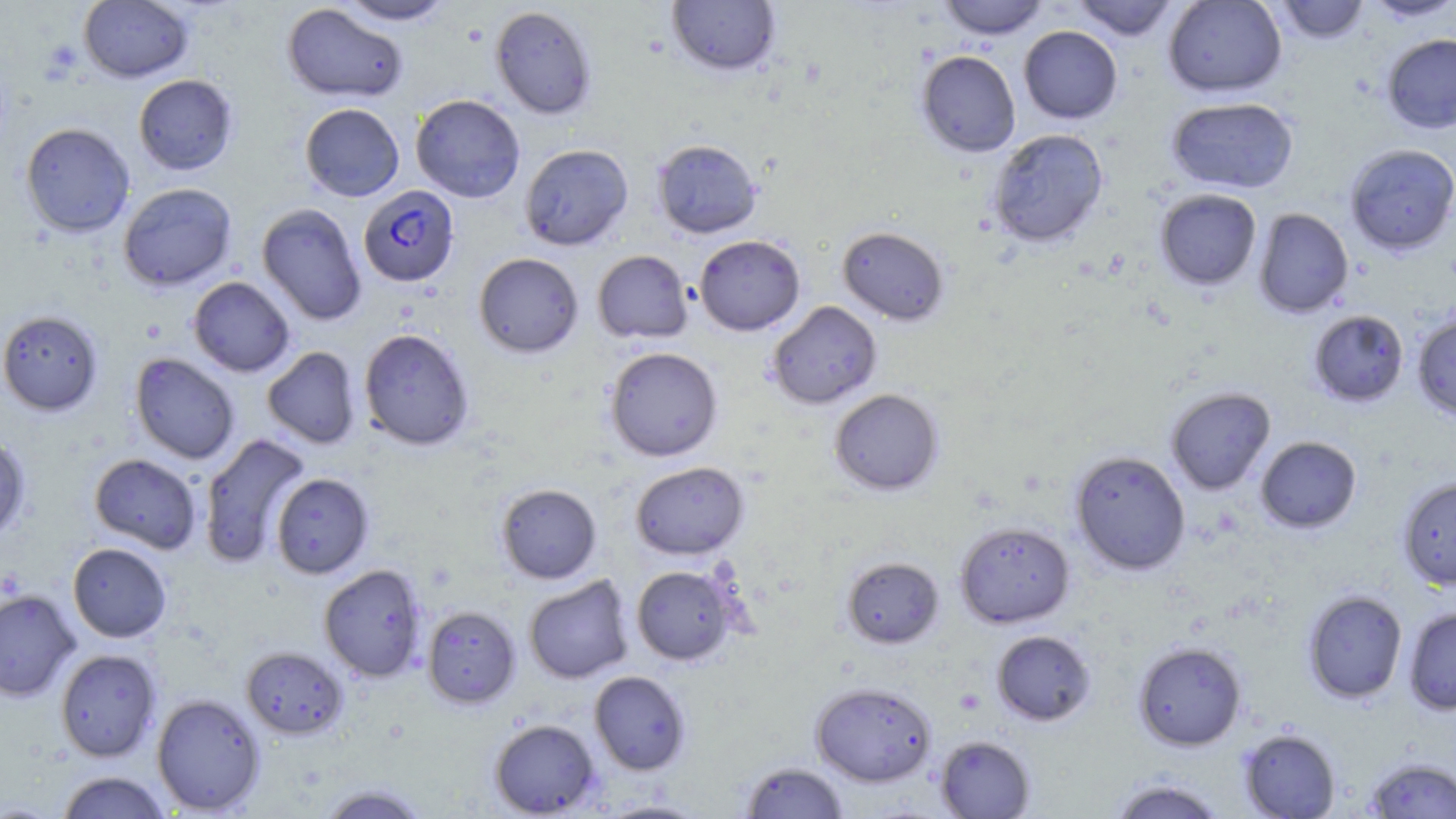
slide-level diagnosis = Plasmodium falciparum
preparation = thin blood smear
uninfected red blood cell locations = approximate bounding boxes as named x1/y1/x2/y2 corners in pixels: (x1=78, y1=0, x2=193, y2=82), (x1=335, y1=0, x2=457, y2=25), (x1=939, y1=0, x2=1048, y2=40), (x1=1071, y1=0, x2=1180, y2=40), (x1=1162, y1=0, x2=1287, y2=98), (x1=1272, y1=0, x2=1370, y2=43), (x1=1361, y1=0, x2=1456, y2=22), (x1=666, y1=1, x2=782, y2=77), (x1=282, y1=3, x2=408, y2=103), (x1=490, y1=5, x2=597, y2=119), (x1=1018, y1=26, x2=1123, y2=124), (x1=1381, y1=33, x2=1456, y2=134), (x1=916, y1=50, x2=1021, y2=157), (x1=133, y1=74, x2=238, y2=175), (x1=410, y1=94, x2=526, y2=203), (x1=1166, y1=97, x2=1299, y2=194), (x1=300, y1=103, x2=404, y2=202), (x1=20, y1=122, x2=135, y2=237), (x1=988, y1=128, x2=1108, y2=247), (x1=652, y1=139, x2=762, y2=238), (x1=1344, y1=143, x2=1456, y2=255), (x1=519, y1=144, x2=633, y2=251), (x1=118, y1=183, x2=237, y2=291), (x1=1154, y1=188, x2=1262, y2=290), (x1=256, y1=203, x2=367, y2=326), (x1=1254, y1=208, x2=1354, y2=318), (x1=837, y1=225, x2=949, y2=326), (x1=694, y1=234, x2=805, y2=335), (x1=593, y1=250, x2=693, y2=343), (x1=474, y1=252, x2=583, y2=358), (x1=188, y1=276, x2=296, y2=377), (x1=767, y1=301, x2=882, y2=409), (x1=0, y1=310, x2=103, y2=416), (x1=1308, y1=310, x2=1409, y2=407), (x1=1412, y1=312, x2=1456, y2=421), (x1=359, y1=328, x2=475, y2=451), (x1=605, y1=346, x2=723, y2=461), (x1=262, y1=347, x2=361, y2=449), (x1=130, y1=353, x2=240, y2=464), (x1=1165, y1=387, x2=1276, y2=495), (x1=829, y1=388, x2=944, y2=495), (x1=0, y1=434, x2=31, y2=543), (x1=198, y1=434, x2=311, y2=567), (x1=1255, y1=436, x2=1362, y2=534), (x1=1070, y1=450, x2=1191, y2=575), (x1=89, y1=453, x2=202, y2=554), (x1=630, y1=461, x2=749, y2=560), (x1=270, y1=473, x2=374, y2=578), (x1=1398, y1=477, x2=1456, y2=589), (x1=496, y1=483, x2=601, y2=584), (x1=954, y1=521, x2=1075, y2=628), (x1=67, y1=542, x2=172, y2=642), (x1=841, y1=556, x2=944, y2=649), (x1=318, y1=564, x2=427, y2=682), (x1=631, y1=564, x2=739, y2=665), (x1=523, y1=575, x2=634, y2=684), (x1=0, y1=589, x2=81, y2=702), (x1=1302, y1=590, x2=1408, y2=703), (x1=422, y1=606, x2=520, y2=708), (x1=1403, y1=606, x2=1456, y2=716), (x1=991, y1=629, x2=1096, y2=726), (x1=1133, y1=641, x2=1246, y2=751), (x1=241, y1=646, x2=348, y2=739), (x1=55, y1=649, x2=161, y2=761), (x1=589, y1=670, x2=691, y2=775), (x1=811, y1=681, x2=936, y2=787), (x1=152, y1=693, x2=266, y2=815), (x1=489, y1=718, x2=600, y2=817), (x1=1238, y1=728, x2=1341, y2=818), (x1=935, y1=735, x2=1035, y2=818), (x1=1363, y1=757, x2=1456, y2=818), (x1=739, y1=761, x2=849, y2=819), (x1=55, y1=770, x2=173, y2=818), (x1=1107, y1=777, x2=1229, y2=819), (x1=315, y1=784, x2=432, y2=819), (x1=596, y1=800, x2=710, y2=818)
modality = optical microscopy
Plasmodium falciparum-infected red blood cell locations = approximate bounding boxes as named x1/y1/x2/y2 corners in pixels: (x1=358, y1=185, x2=459, y2=287)
platelet locations = approximate bounding boxes as named x1/y1/x2/y2 corners in pixels: (x1=42, y1=41, x2=82, y2=80)
stain = May-Grünwald-Giemsa
field of view = single
magnification = 1000x
image size = 1456×819 pixels